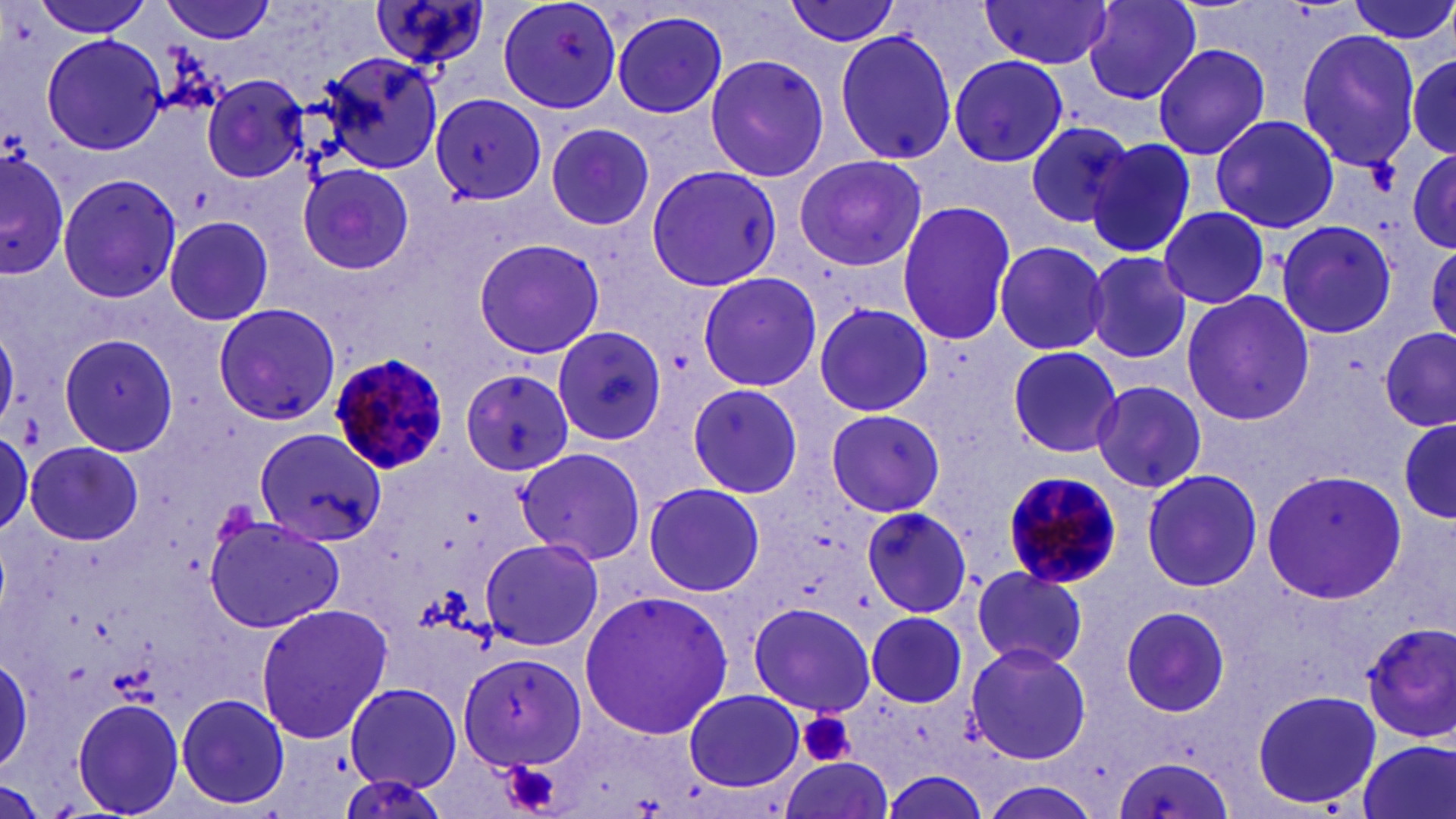
slide_level_diagnosis: Plasmodium malariae
modality: light microscopy
field_of_view: one of a larger specimen
preparation: thin blood smear
plasmodium_malariae_infected_red_blood_cell_locations: 'approximate bounding boxes as [x1, y1, x2, y2] in pixels: [330, 352, 453, 476], [1000, 468, 1126, 599]'
platelet_locations: 'approximate bounding boxes as [x1, y1, x2, y2] in pixels: [798, 711, 856, 769], [498, 759, 566, 818]'
magnification: 1000x
image_size: 1456×819 pixels
uninfected_red_blood_cell_locations: 'approximate bounding boxes as [x1, y1, x2, y2] in pixels: [30, 0, 154, 38], [158, 0, 278, 43], [368, 0, 494, 77], [497, 0, 623, 114], [783, 0, 906, 47], [1082, 0, 1203, 105], [1343, 0, 1456, 46], [979, 1, 1112, 71], [612, 11, 729, 119], [832, 27, 957, 167], [1295, 27, 1422, 174], [42, 33, 166, 156], [1152, 43, 1272, 160], [1402, 46, 1456, 163], [314, 49, 446, 175], [704, 55, 832, 183], [949, 55, 1068, 167], [199, 73, 311, 183], [431, 95, 546, 204], [1210, 114, 1341, 234], [1025, 120, 1134, 228], [545, 122, 655, 231], [1086, 136, 1197, 260], [2, 147, 70, 280], [1408, 149, 1456, 252], [1409, 149, 1455, 251], [793, 154, 927, 272], [298, 163, 414, 276], [645, 164, 783, 290], [56, 172, 183, 305], [895, 199, 1018, 348], [1158, 206, 1270, 308], [164, 216, 276, 327], [1273, 219, 1396, 340], [471, 239, 605, 359], [991, 241, 1108, 355], [1428, 241, 1456, 344], [1083, 249, 1194, 367], [696, 271, 822, 392], [1179, 290, 1315, 427], [211, 302, 340, 427], [814, 303, 932, 419], [550, 325, 666, 446], [1374, 326, 1455, 443], [1379, 328, 1454, 433], [0, 330, 23, 431], [57, 332, 180, 458], [1006, 345, 1123, 459], [461, 368, 575, 475], [1090, 379, 1207, 493], [686, 382, 803, 498], [825, 409, 948, 518], [1397, 418, 1453, 524], [0, 427, 32, 540], [253, 429, 387, 548], [26, 441, 142, 544], [516, 445, 647, 566], [1260, 467, 1406, 605], [1141, 468, 1263, 593], [642, 482, 765, 598], [861, 505, 976, 617], [205, 514, 343, 633], [479, 537, 604, 649], [969, 568, 1088, 669], [576, 587, 736, 742], [747, 601, 876, 717], [254, 603, 393, 744], [1116, 603, 1232, 718], [864, 610, 968, 709], [1361, 619, 1456, 743], [964, 641, 1093, 765], [0, 651, 33, 771], [458, 652, 586, 770], [342, 681, 466, 796], [683, 688, 804, 791], [1250, 688, 1383, 811], [175, 693, 291, 811], [70, 697, 185, 817], [1355, 738, 1455, 819], [1110, 756, 1234, 819], [778, 759, 891, 819], [881, 772, 989, 818], [973, 778, 1104, 819]'
stain: May-Grünwald-Giemsa